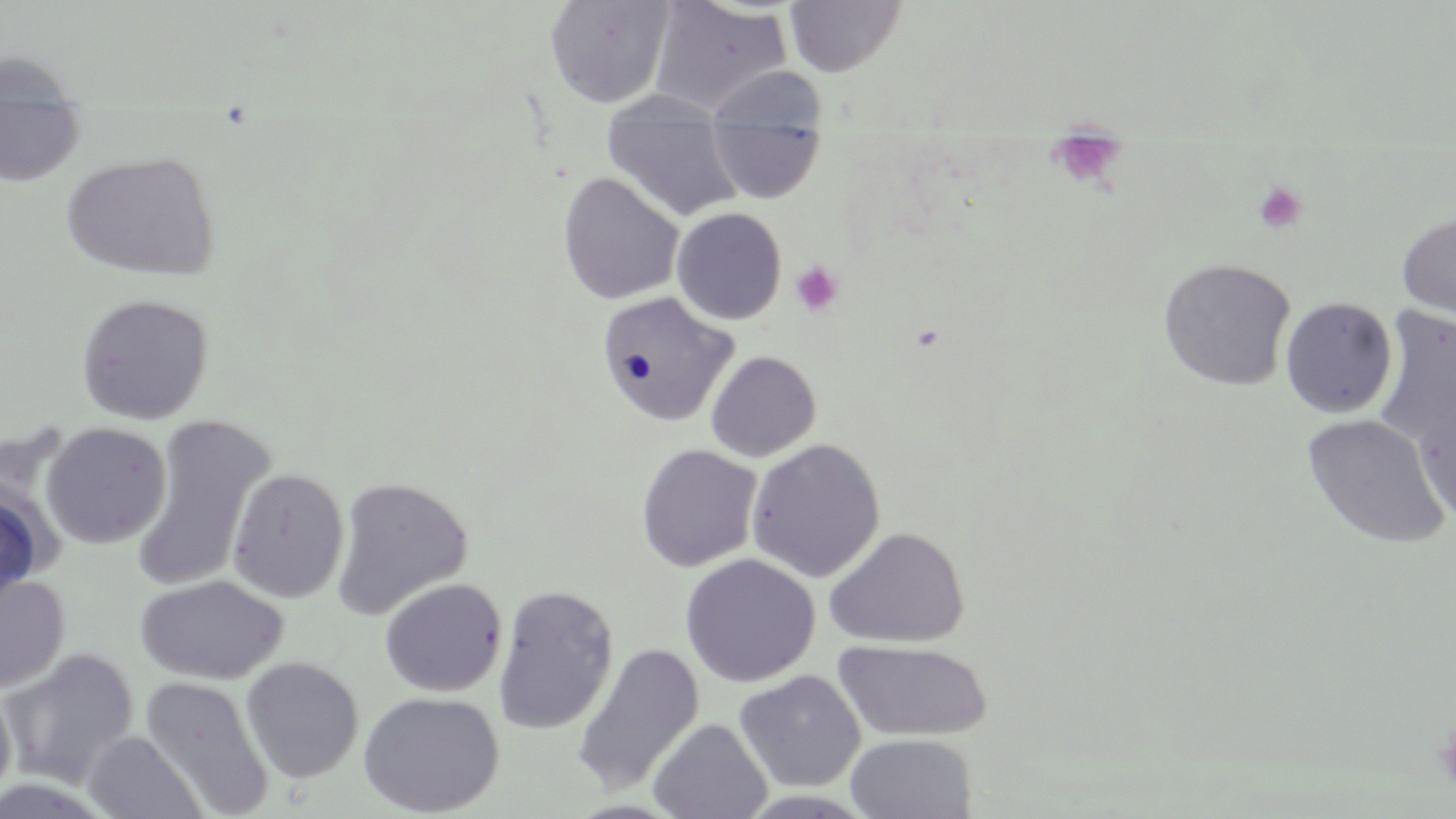
Summary:
  - Coordinate format: approximate bounding boxes as (x1,y1)-(x2,y2) corner pairs in pixels
  - Platelet locations: (1046,136)-(1129,188), (1253,181)-(1308,235), (790,261)-(843,317), (1435,723)-(1456,789)
  - Uninfected red blood cell locations: (544,0)-(675,109), (784,0)-(906,77), (649,1)-(792,116), (0,49)-(83,104), (601,91)-(743,222), (0,106)-(84,185), (706,115)-(825,203), (61,150)-(221,281), (557,172)-(685,305), (672,207)-(787,325), (1397,212)-(1456,319), (1158,258)-(1296,391), (596,291)-(738,427), (75,293)-(214,425), (1280,297)-(1398,419), (1372,305)-(1456,448), (705,350)-(822,462), (1413,394)-(1456,528), (1302,414)-(1451,549), (132,416)-(275,592), (41,422)-(171,548), (746,438)-(886,583), (636,444)-(762,573), (226,468)-(349,603), (331,476)-(472,620), (0,490)-(46,610), (825,526)-(969,649), (679,553)-(821,688), (0,574)-(69,693), (134,575)-(289,685), (379,578)-(507,697), (492,583)-(619,735), (833,639)-(993,742), (572,643)-(705,795), (0,648)-(139,789), (240,657)-(364,783), (733,670)-(866,792), (139,675)-(274,818), (0,679)-(16,809), (358,691)-(505,817), (647,718)-(773,819), (80,731)-(207,818), (844,733)-(977,819), (735,790)-(879,818)
  - Slide-level diagnosis: negative for blood parasites
  - Image size: 1456×819 pixels
  - Stain: May-Grünwald-Giemsa
  - Field of view: single
  - Preparation: thin blood film
  - Modality: light microscopy
  - Magnification: 1000x